Identify the cell.
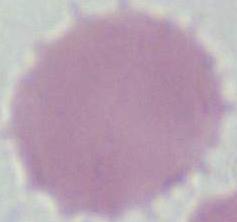

This is an erythrocyte.

1000x magnification. Micrograph.